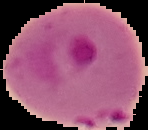
image_size: 148×130 pixels
image_type: cell region segmented out of the field of view; surrounding area masked to black
malaria_status: parasitized
preparation: thin blood smear